Report the malaria status of this cell.
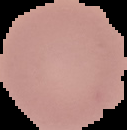
It is uninfected.

From a thin blood film. Image is 127×130 pixels. Segmented cell region on a black background.